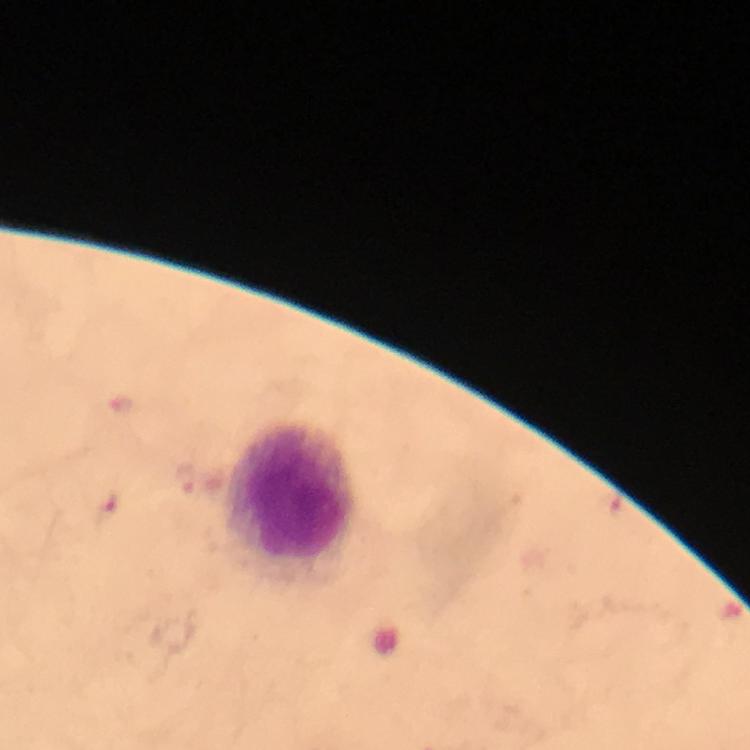

Approximate centers as (x, y) in pixels.
Summary:
  - Leukocyte locations: (289, 494)
  - Preparation: thick blood film
  - Context: from a malaria diagnostic workup
  - Malaria parasites: none detected
  - Image size: 750×750 pixels
  - Stain: Giemsa
  - Immersion oil: used
  - Magnification: 100x
  - Cropped from: a single field of view
  - Capture: smartphone camera through the microscope